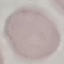
Summary:
  - Malaria status: uninfected
  - Image type: cell patch, automatically extracted from a larger field of view and resized to 64 × 64 pixels
  - Preparation: thin blood smear
  - Stain: Giemsa
  - Capture: smartphone through the microscope eyepiece